Name the parasite shown.
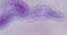

A trypanosome.

{
  "magnification": "1000x",
  "modality": "micrograph"
}